Report the malaria status of this cell.
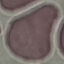
It is uninfected.

image_type: cell patch, automatically extracted from a larger field of view and resized to 64 × 64 pixels
capture: smartphone camera at the microscope eyepiece
preparation: thin smear
stain: Giemsa